Classify this cell by malaria status.
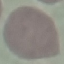
Uninfected.

preparation = thin blood film
stain = Giemsa
image type = cell patch, automatically extracted from a larger field of view and resized to 64 × 64 pixels
capture = smartphone through the microscope eyepiece